Name the blood parasite species.
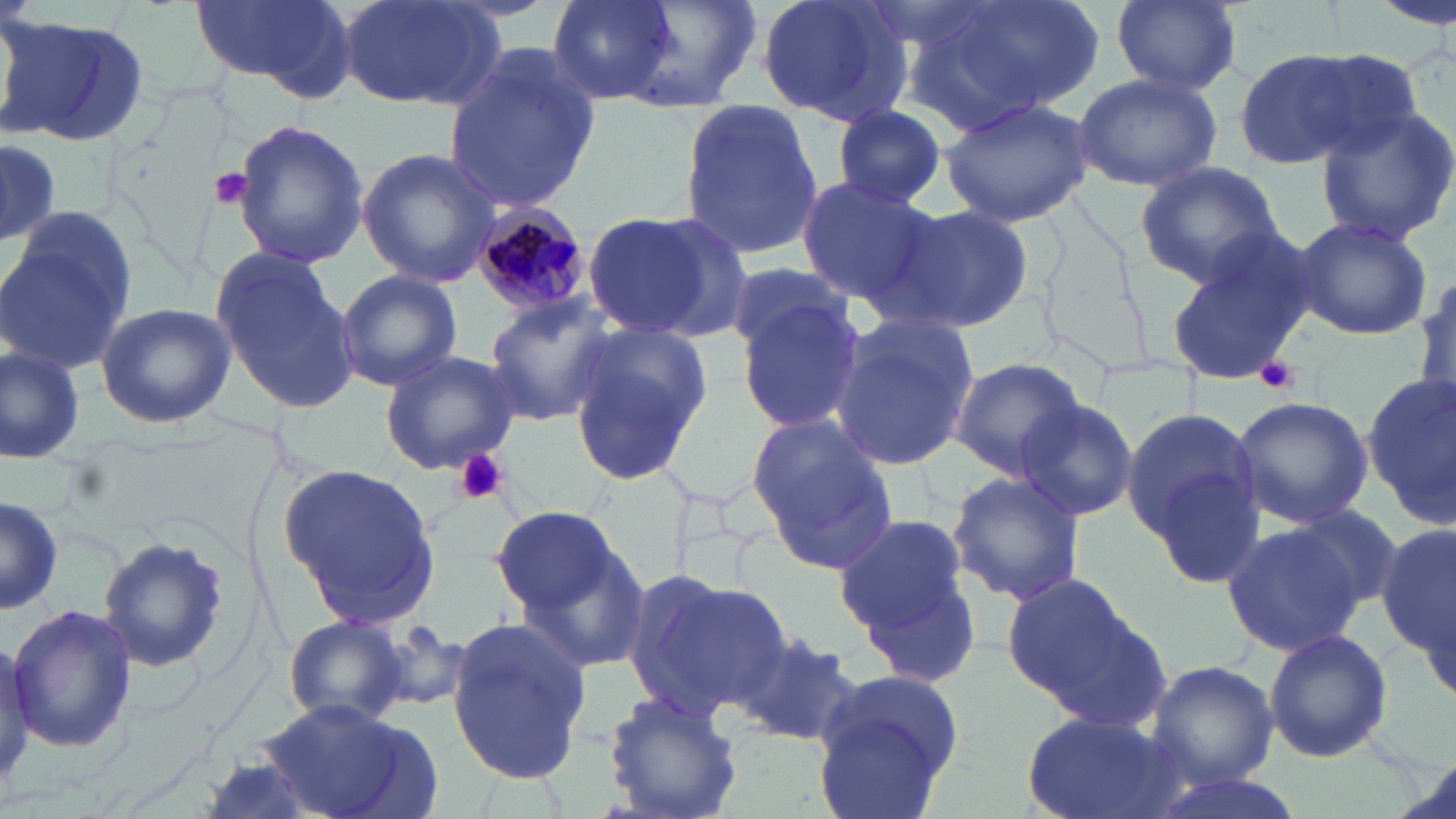
Plasmodium malariae.

Summary:
  - Coordinate format: approximate bounding boxes as [x1, y1, x2, y2] in pixels
  - Uninfected red blood cell locations: [188, 0, 352, 95], [334, 0, 507, 110], [545, 0, 678, 103], [595, 0, 763, 111], [756, 0, 915, 126], [907, 0, 1102, 130], [1375, 0, 1450, 27], [1110, 1, 1240, 95], [0, 15, 151, 149], [439, 48, 598, 216], [1233, 48, 1371, 171], [1072, 71, 1222, 192], [938, 97, 1096, 227], [677, 98, 826, 264], [829, 105, 952, 208], [1312, 105, 1456, 245], [229, 119, 370, 268], [0, 137, 61, 248], [357, 147, 501, 287], [1132, 159, 1285, 287], [793, 175, 939, 306], [897, 206, 1033, 330], [584, 207, 749, 342], [2, 208, 140, 376], [1289, 214, 1433, 341], [1164, 229, 1319, 386], [207, 250, 358, 408], [723, 263, 857, 365], [333, 269, 462, 393], [1414, 272, 1455, 411], [733, 294, 866, 435], [482, 296, 617, 426], [94, 303, 235, 428], [829, 313, 979, 473], [567, 322, 710, 476], [0, 343, 86, 464], [379, 350, 521, 473], [947, 357, 1087, 479], [1363, 372, 1456, 522], [1233, 395, 1374, 529], [1014, 397, 1138, 521], [1122, 401, 1263, 570], [748, 416, 900, 572], [280, 465, 442, 625], [947, 468, 1088, 608], [0, 494, 62, 619], [1280, 503, 1409, 621], [490, 506, 621, 616], [833, 511, 981, 681], [1219, 521, 1368, 656], [1375, 523, 1455, 665], [97, 534, 230, 676], [508, 536, 651, 671], [625, 571, 790, 723], [1001, 574, 1153, 713], [7, 602, 137, 754], [283, 616, 412, 727], [446, 617, 589, 785], [369, 624, 474, 713], [1, 625, 38, 805], [731, 629, 862, 746], [1263, 629, 1394, 762], [1145, 659, 1279, 789], [809, 667, 968, 815], [604, 691, 743, 819], [254, 700, 437, 816], [1022, 712, 1186, 819], [1140, 768, 1307, 819]
  - Plasmodium malariae-infected red blood cell locations: [471, 209, 595, 319]
  - Platelet locations: [207, 167, 254, 210], [1255, 359, 1300, 396], [452, 448, 508, 505]
  - Field of view: single
  - Modality: optical microscopy
  - Stain: May-Grünwald-Giemsa
  - Preparation: thin blood film
  - Magnification: 1000x
  - Image size: 1456×819 pixels